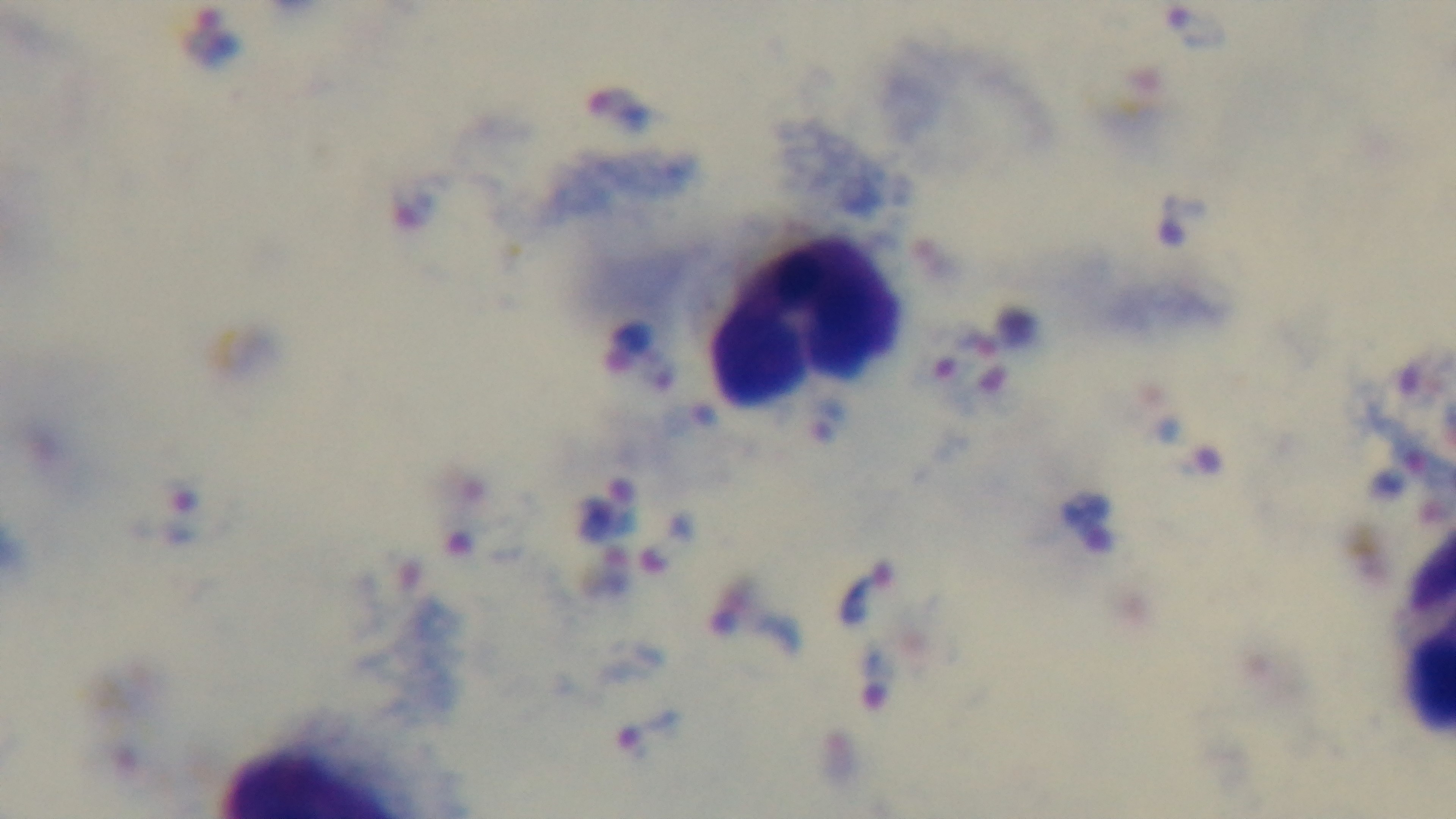

{
  "capture": "mounted 4K digital camera",
  "modality": "light microscopy",
  "preparation": "thick smear",
  "malaria_status": "infected",
  "field_of_view": "single",
  "stain": "Giemsa",
  "objective": "100x oil immersion"
}